Locate every Plasmodium parasite.
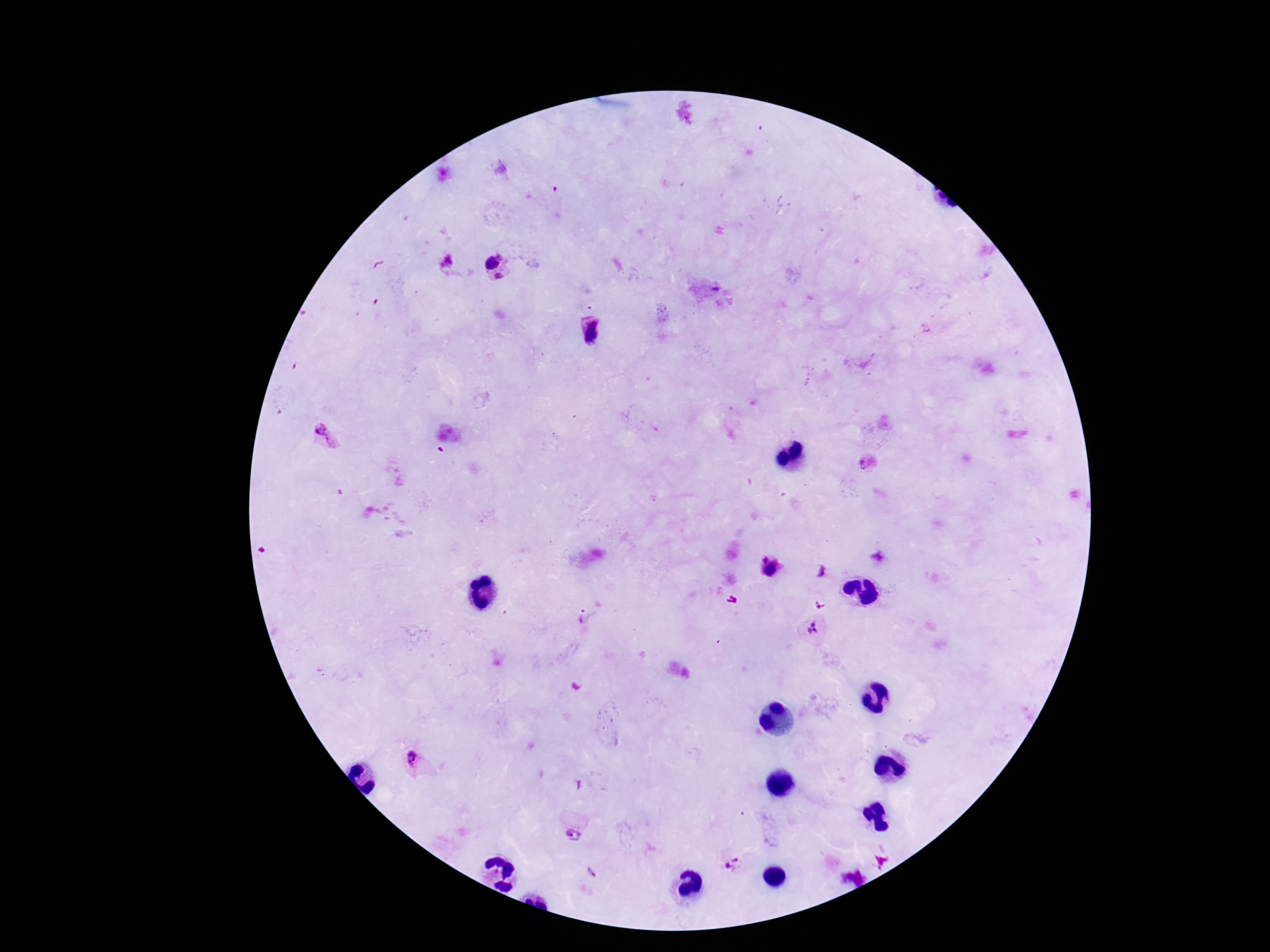
Approximate centers as (x, y) in pixels.
Plasmodium parasites: (501, 255), (448, 261), (491, 263), (499, 276), (714, 289), (589, 332), (327, 437), (863, 464), (654, 497), (764, 558), (772, 569), (813, 624), (808, 630), (815, 631), (415, 764), (573, 835), (734, 860), (728, 865), (590, 871).

{
  "stain": "Giemsa",
  "magnification": "100x",
  "preparation": "thick blood film",
  "image_size": "1270×952 pixels",
  "patient_malaria_status": "infected",
  "field_of_view": "one from this slide",
  "capture": "smartphone camera through the microscope eyepiece"
}